State which cell type is depicted.
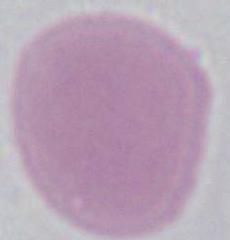

An erythrocyte.

Summary:
  - Modality: photomicrograph
  - Magnification: 1000x